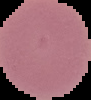
{
  "malaria_status": "uninfected",
  "image_type": "cell region segmented out of the field of view; surrounding area masked to black",
  "preparation": "thin blood film",
  "image_size": "91×100 pixels"
}